Give the extent of all Plasmodium malariae-infected red blood cells.
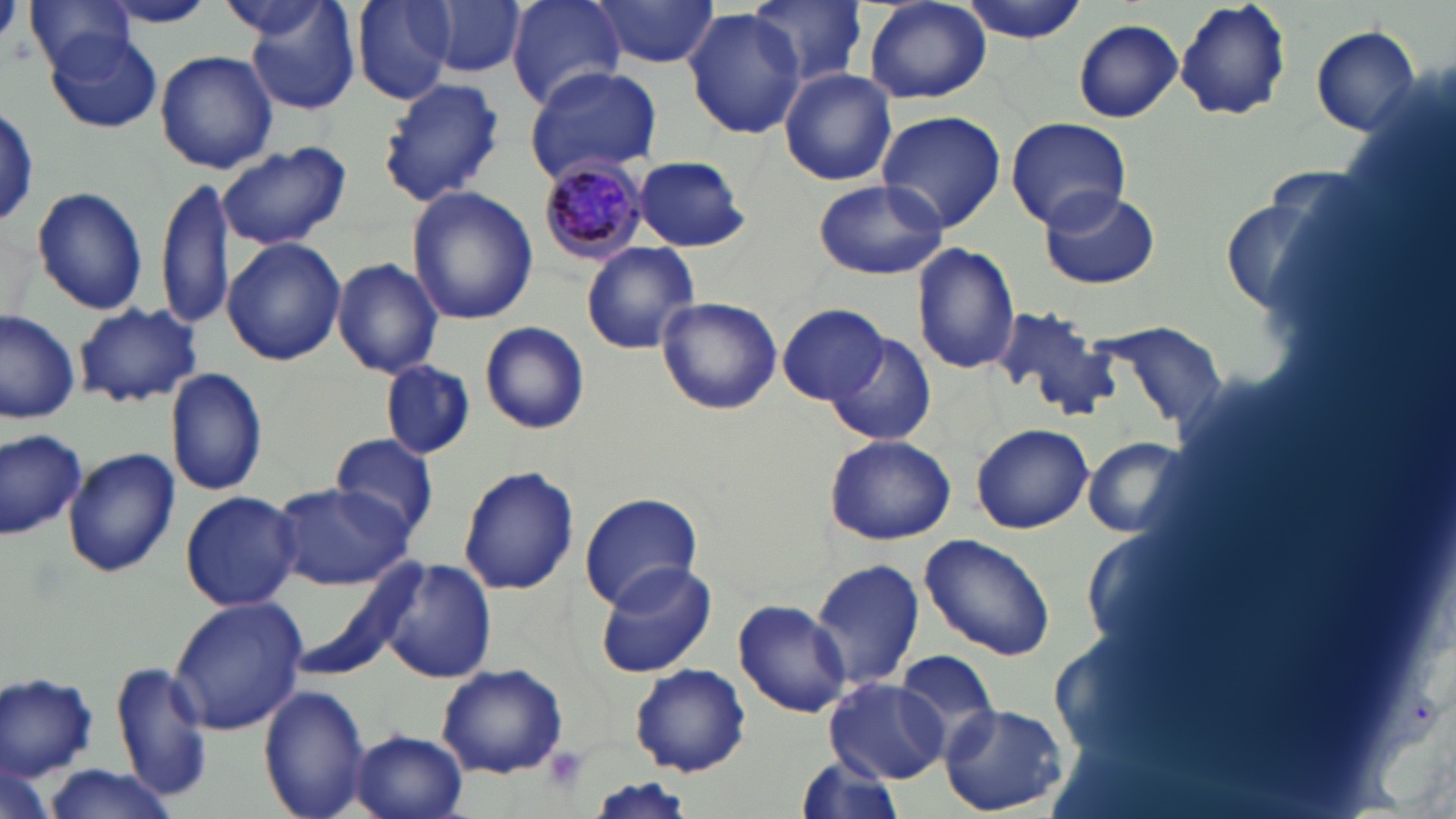
Approximate bounding boxes as (x1, y1, x2, y2) in pixels.
Plasmodium malariae-infected red blood cells: (535, 155, 653, 262).

Uninfected red blood cell locations: (25, 0, 137, 79), (354, 0, 455, 103), (422, 0, 526, 77), (508, 0, 627, 107), (589, 0, 721, 69), (960, 0, 1094, 41), (1174, 0, 1291, 121), (103, 1, 215, 27), (747, 1, 868, 86), (863, 1, 992, 105), (214, 2, 336, 40), (240, 2, 363, 115), (682, 9, 807, 139), (1073, 19, 1183, 123), (1312, 27, 1423, 137), (47, 32, 163, 134), (153, 49, 279, 176), (522, 65, 662, 185), (777, 69, 899, 187), (377, 77, 508, 208), (875, 109, 1007, 233), (1005, 117, 1131, 230), (216, 140, 352, 254), (633, 155, 749, 251), (156, 173, 232, 336), (812, 178, 948, 281), (30, 186, 149, 316), (1038, 186, 1160, 290), (405, 187, 538, 326), (1222, 196, 1338, 315), (222, 237, 345, 366), (580, 242, 699, 355), (913, 243, 1020, 374), (333, 258, 444, 378), (656, 296, 783, 416), (73, 300, 203, 407), (779, 304, 887, 404), (990, 304, 1116, 422), (0, 307, 82, 424), (481, 321, 589, 435), (1099, 321, 1229, 424), (826, 331, 935, 446), (379, 361, 474, 459), (166, 367, 267, 497), (970, 423, 1093, 534), (0, 429, 87, 539), (327, 433, 440, 539), (825, 433, 956, 545), (1080, 436, 1194, 541), (63, 448, 181, 578), (458, 467, 580, 596), (270, 480, 414, 591), (180, 491, 302, 611), (578, 493, 702, 611), (922, 534, 1057, 661), (374, 558, 498, 684), (810, 558, 924, 695), (593, 561, 719, 678), (169, 596, 307, 736), (734, 599, 851, 718), (892, 648, 1003, 752), (110, 659, 212, 801), (437, 662, 568, 778), (631, 664, 751, 776), (1, 672, 99, 780), (825, 679, 950, 782), (259, 684, 371, 818), (940, 703, 1069, 815), (351, 729, 468, 819), (792, 753, 910, 817), (35, 763, 185, 818). Platelet locations: (0, 0, 21, 45), (543, 745, 590, 796). Slide-level diagnosis: Plasmodium malariae. Optical microscopy. May-Grünwald-Giemsa-stained preparation. Single field of view. Thin blood smear. 1000x magnification. Image is 1456×819 pixels.